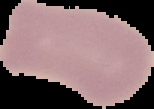
Summary:
  - Image size: 154×109 pixels
  - Image type: segmented cell region on a black background
  - Preparation: thin blood film
  - Malaria status: uninfected